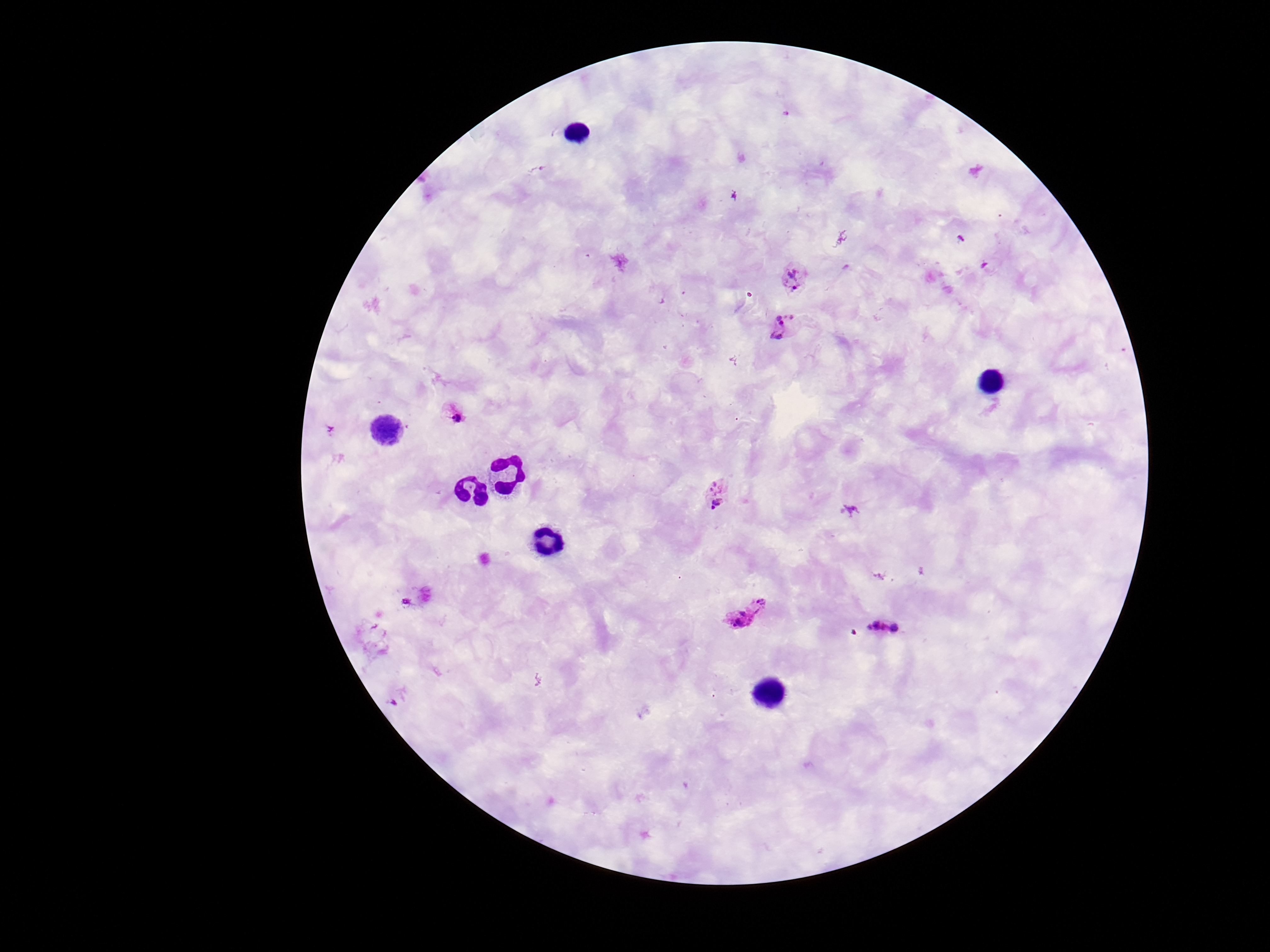
Approximate centers as (x, y) in pixels.
Summary:
  - Plasmodium parasite locations: (796, 276), (784, 326), (453, 413), (719, 494), (747, 614), (883, 627)
  - Magnification: 100x
  - Patient malaria status: infected
  - Preparation: thick blood film
  - Stain: Giemsa
  - Field of view: one from this slide
  - Capture: smartphone camera through the microscope eyepiece
  - Image size: 1270×952 pixels